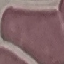

{
  "result": "no malaria parasites detected",
  "preparation": "thin blood film",
  "image_type": "automatically extracted cell patch, resized to 64 × 64 pixels",
  "stain": "Giemsa",
  "capture": "smartphone through the microscope eyepiece"
}